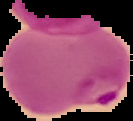
image size = 133×121 pixels
malaria status = parasitized
preparation = thin blood film
image type = segmented cell region on a black background